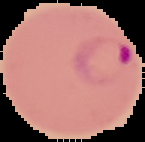

image type = segmented cell region with the area outside set to black
preparation = thin blood film
image size = 145×142 pixels
malaria status = parasitized